Report the malaria status of this cell.
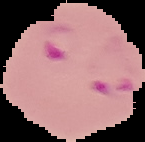

Parasitized.

Image is 145×142 pixels. Segmented cell region on a black background. From a thin blood film.